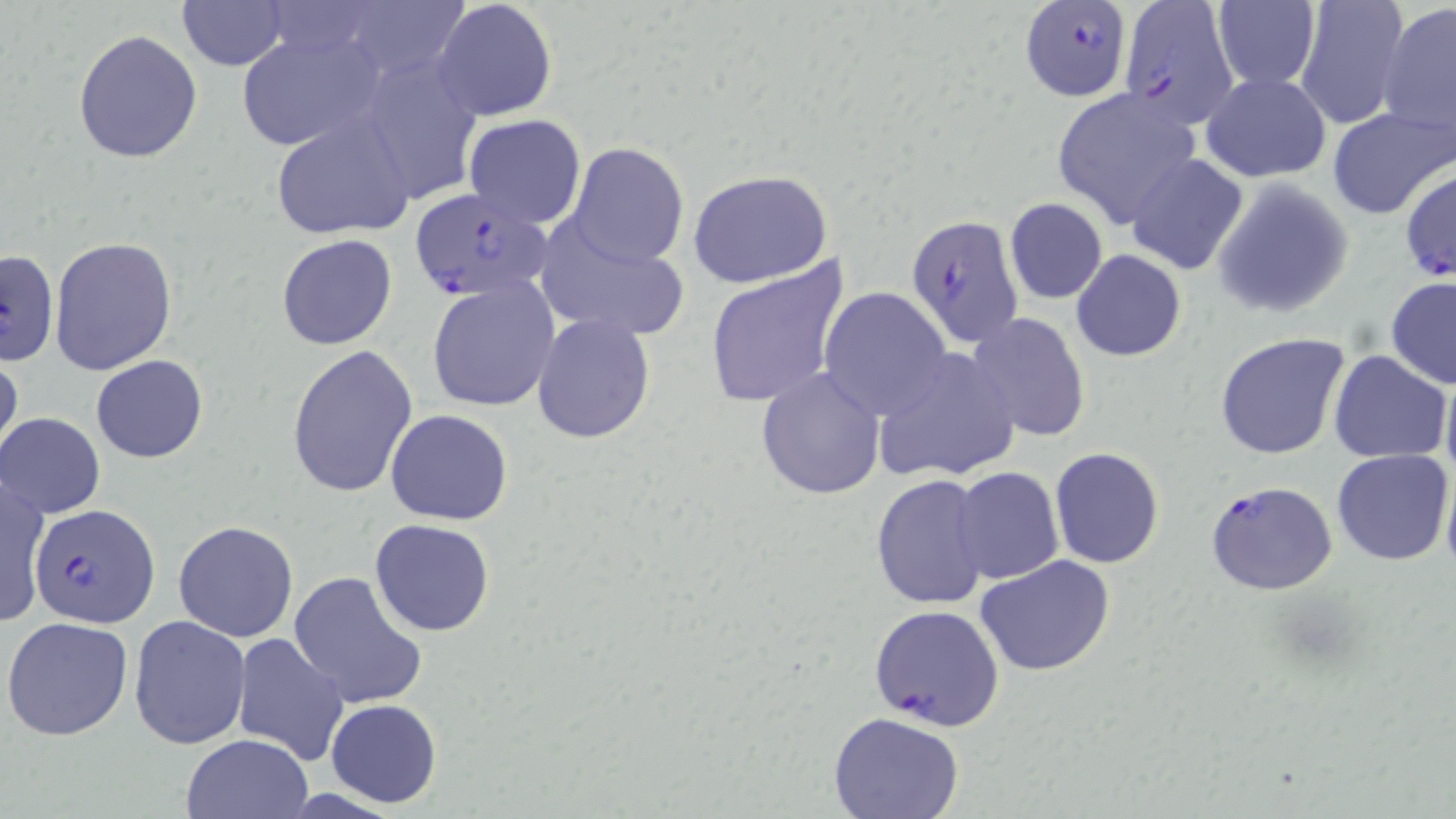
slide-level diagnosis = Plasmodium falciparum
image size = 1456×819 pixels
field of view = one of a larger specimen
stain = May-Grünwald-Giemsa
magnification = 1000x
modality = optical microscopy
Plasmodium falciparum-infected red blood cell locations = approximate bounding boxes as (x1, y1, x2, y2) in pixels: (1117, 0, 1238, 124), (1020, 1, 1132, 101), (1399, 167, 1455, 284), (408, 188, 554, 303), (906, 212, 1024, 351), (1205, 480, 1338, 596), (31, 504, 158, 628), (867, 604, 1006, 732)
preparation = thin blood film
uninfected red blood cell locations = approximate bounding boxes as (x1, y1, x2, y2) in pixels: (176, 0, 290, 71), (1294, 0, 1409, 129), (1210, 1, 1321, 93), (430, 2, 557, 122), (1378, 3, 1456, 141), (236, 28, 387, 153), (73, 29, 203, 162), (347, 50, 488, 207), (1200, 72, 1330, 183), (1052, 89, 1203, 227), (1326, 106, 1453, 219), (463, 114, 586, 228), (270, 115, 416, 241), (566, 142, 690, 267), (1126, 153, 1250, 275), (688, 169, 833, 289), (1212, 178, 1355, 319), (1005, 198, 1107, 304), (531, 220, 690, 342), (276, 234, 398, 350), (49, 236, 178, 377), (0, 249, 60, 367), (1072, 249, 1186, 361), (702, 259, 850, 409), (1386, 276, 1456, 389), (428, 279, 559, 413), (819, 287, 952, 419), (967, 312, 1091, 443), (531, 315, 656, 443), (1214, 333, 1351, 461), (286, 345, 417, 498), (872, 349, 1022, 484), (1329, 350, 1452, 462), (0, 351, 24, 472), (91, 354, 208, 464), (757, 367, 887, 500), (1440, 367, 1456, 495), (385, 409, 514, 525), (1, 413, 105, 518), (1050, 448, 1164, 569), (1332, 448, 1452, 566), (952, 467, 1063, 584), (1441, 467, 1456, 584), (869, 474, 994, 611), (0, 477, 51, 627), (368, 519, 496, 637), (173, 521, 299, 642), (976, 554, 1117, 677), (287, 571, 430, 710), (129, 614, 251, 748), (2, 616, 134, 741), (229, 630, 352, 766), (325, 698, 442, 808), (827, 713, 967, 819), (181, 733, 313, 818)